Outline each blood parasite and name the species.
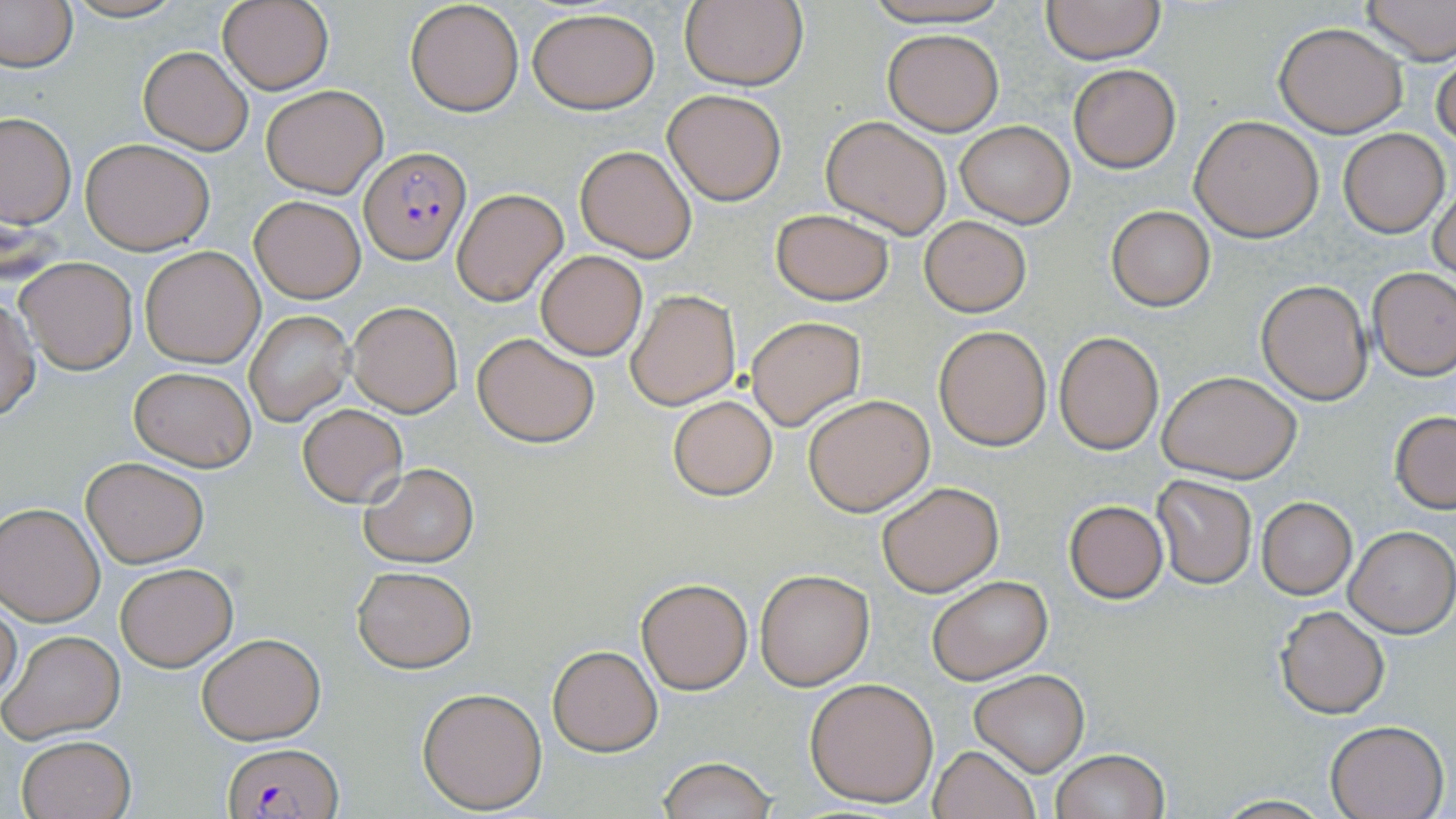
Approximate bounding boxes as named x1/y1/x2/y2 corners in pixels.
Plasmodium falciparum-infected red blood cells: (x1=361, y1=146, x2=471, y2=263), (x1=223, y1=742, x2=341, y2=819).
No Plasmodium ovale, Plasmodium malariae, Plasmodium vivax, Babesia divergens, or Trypanosoma brucei observed.

{
  "slide_level_diagnosis": "Plasmodium falciparum",
  "preparation": "thin blood film",
  "magnification": "1000x",
  "uninfected_red_blood_cell_locations": "approximate bounding boxes as named x1/y1/x2/y2 corners in pixels: (x1=61, y1=0, x2=189, y2=23), (x1=405, y1=0, x2=526, y2=117), (x1=863, y1=0, x2=1012, y2=27), (x1=1039, y1=0, x2=1167, y2=66), (x1=1357, y1=0, x2=1455, y2=65), (x1=0, y1=1, x2=78, y2=73), (x1=216, y1=1, x2=333, y2=92), (x1=678, y1=1, x2=808, y2=90), (x1=527, y1=7, x2=661, y2=112), (x1=1274, y1=22, x2=1408, y2=137), (x1=882, y1=29, x2=1003, y2=135), (x1=139, y1=46, x2=253, y2=155), (x1=1433, y1=51, x2=1455, y2=157), (x1=1067, y1=64, x2=1181, y2=171), (x1=261, y1=83, x2=388, y2=198), (x1=662, y1=89, x2=787, y2=205), (x1=0, y1=112, x2=75, y2=227), (x1=1190, y1=115, x2=1325, y2=241), (x1=821, y1=116, x2=953, y2=238), (x1=955, y1=121, x2=1074, y2=227), (x1=1340, y1=129, x2=1449, y2=236), (x1=81, y1=137, x2=216, y2=254), (x1=574, y1=143, x2=699, y2=262), (x1=1428, y1=175, x2=1456, y2=283), (x1=452, y1=189, x2=568, y2=306), (x1=251, y1=195, x2=365, y2=303), (x1=1105, y1=205, x2=1216, y2=311), (x1=769, y1=208, x2=896, y2=306), (x1=919, y1=216, x2=1031, y2=316), (x1=140, y1=246, x2=265, y2=367), (x1=534, y1=249, x2=648, y2=360), (x1=16, y1=256, x2=138, y2=374), (x1=1367, y1=266, x2=1456, y2=380), (x1=1256, y1=279, x2=1374, y2=405), (x1=625, y1=289, x2=740, y2=410), (x1=0, y1=294, x2=39, y2=421), (x1=348, y1=301, x2=462, y2=417), (x1=245, y1=310, x2=354, y2=425), (x1=746, y1=316, x2=865, y2=430), (x1=932, y1=326, x2=1052, y2=449), (x1=1054, y1=332, x2=1164, y2=454), (x1=472, y1=333, x2=601, y2=446), (x1=129, y1=364, x2=256, y2=472), (x1=1157, y1=370, x2=1301, y2=484), (x1=804, y1=393, x2=935, y2=516), (x1=667, y1=395, x2=778, y2=499), (x1=298, y1=404, x2=407, y2=508), (x1=1390, y1=411, x2=1456, y2=512), (x1=81, y1=457, x2=210, y2=567), (x1=359, y1=463, x2=480, y2=567), (x1=1152, y1=473, x2=1257, y2=588), (x1=877, y1=481, x2=1004, y2=597), (x1=1256, y1=498, x2=1357, y2=599), (x1=1064, y1=500, x2=1169, y2=603), (x1=0, y1=501, x2=105, y2=625), (x1=1344, y1=527, x2=1454, y2=637), (x1=114, y1=563, x2=237, y2=671), (x1=351, y1=566, x2=475, y2=673), (x1=755, y1=569, x2=874, y2=690), (x1=926, y1=574, x2=1052, y2=684), (x1=636, y1=575, x2=754, y2=695), (x1=1, y1=597, x2=22, y2=705), (x1=1275, y1=606, x2=1390, y2=719), (x1=1, y1=630, x2=126, y2=743), (x1=196, y1=632, x2=325, y2=744), (x1=548, y1=645, x2=662, y2=755), (x1=968, y1=670, x2=1089, y2=774), (x1=805, y1=677, x2=940, y2=806), (x1=417, y1=686, x2=548, y2=813), (x1=1325, y1=719, x2=1450, y2=819), (x1=16, y1=733, x2=137, y2=819), (x1=928, y1=745, x2=1040, y2=819), (x1=1050, y1=749, x2=1169, y2=819), (x1=656, y1=757, x2=778, y2=818), (x1=1209, y1=794, x2=1333, y2=818)",
  "image_size": "1456×819 pixels",
  "modality": "optical microscopy",
  "field_of_view": "single",
  "stain": "May-Grünwald-Giemsa"
}